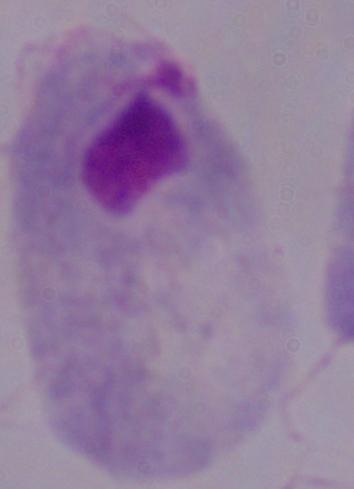
magnification: 1000x
modality: photomicrograph
identification: trichomonad